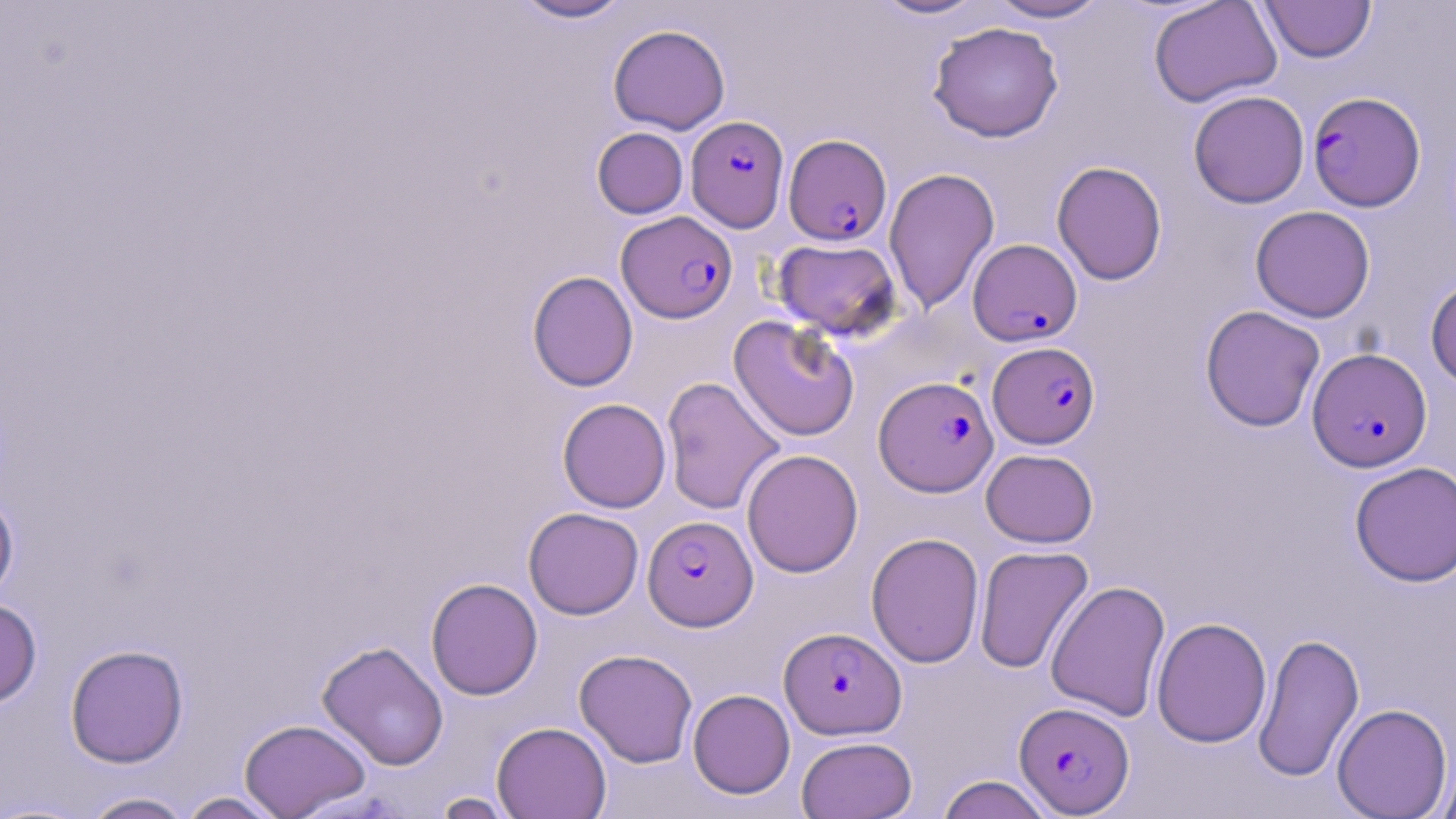

slide-level diagnosis = Plasmodium falciparum
magnification = 1000x
Plasmodium falciparum-infected red blood cell locations = approximate bounding boxes as named x1/y1/x2/y2 corners in pixels: (x1=1307, y1=91, x2=1426, y2=211), (x1=686, y1=115, x2=789, y2=231), (x1=784, y1=133, x2=892, y2=245), (x1=617, y1=211, x2=737, y2=323), (x1=968, y1=238, x2=1082, y2=346), (x1=988, y1=341, x2=1100, y2=448), (x1=1307, y1=348, x2=1432, y2=470), (x1=873, y1=376, x2=998, y2=496), (x1=643, y1=515, x2=758, y2=631), (x1=780, y1=626, x2=906, y2=740), (x1=1014, y1=701, x2=1134, y2=815)
image size = 1456×819 pixels
preparation = thin blood film
stain = May-Grünwald-Giemsa
uninfected red blood cell locations = approximate bounding boxes as named x1/y1/x2/y2 corners in pixels: (x1=511, y1=0, x2=634, y2=23), (x1=871, y1=0, x2=991, y2=20), (x1=986, y1=0, x2=1110, y2=23), (x1=1148, y1=0, x2=1282, y2=107), (x1=1259, y1=1, x2=1376, y2=63), (x1=927, y1=22, x2=1064, y2=142), (x1=608, y1=24, x2=730, y2=134), (x1=1188, y1=90, x2=1309, y2=208), (x1=592, y1=127, x2=688, y2=219), (x1=1051, y1=161, x2=1167, y2=285), (x1=884, y1=167, x2=1000, y2=314), (x1=1250, y1=205, x2=1375, y2=322), (x1=772, y1=238, x2=902, y2=340), (x1=527, y1=270, x2=638, y2=392), (x1=1425, y1=275, x2=1456, y2=389), (x1=1200, y1=305, x2=1325, y2=432), (x1=728, y1=316, x2=860, y2=442), (x1=661, y1=376, x2=785, y2=515), (x1=558, y1=398, x2=671, y2=513), (x1=741, y1=449, x2=863, y2=578), (x1=981, y1=449, x2=1098, y2=547), (x1=1350, y1=461, x2=1456, y2=587), (x1=0, y1=488, x2=19, y2=606), (x1=523, y1=507, x2=644, y2=620), (x1=866, y1=532, x2=984, y2=669), (x1=974, y1=545, x2=1094, y2=673), (x1=425, y1=577, x2=543, y2=700), (x1=1045, y1=580, x2=1170, y2=722), (x1=0, y1=598, x2=42, y2=708), (x1=1152, y1=617, x2=1272, y2=748), (x1=1252, y1=631, x2=1365, y2=783), (x1=317, y1=640, x2=449, y2=770), (x1=65, y1=644, x2=188, y2=768), (x1=574, y1=648, x2=698, y2=768), (x1=688, y1=689, x2=795, y2=799), (x1=1332, y1=702, x2=1452, y2=818), (x1=239, y1=718, x2=371, y2=818), (x1=492, y1=721, x2=612, y2=819), (x1=797, y1=735, x2=917, y2=819), (x1=1436, y1=757, x2=1456, y2=819), (x1=936, y1=774, x2=1056, y2=819), (x1=430, y1=791, x2=522, y2=819), (x1=79, y1=792, x2=195, y2=819), (x1=177, y1=792, x2=288, y2=818)
field of view = one of a larger specimen
modality = light microscopy